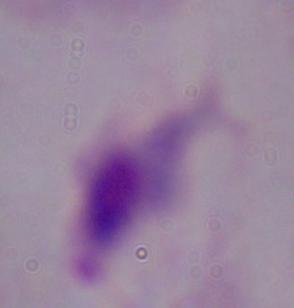
modality = photomicrograph
magnification = 1000x
identification = trichomonad